Assess this cell for malaria.
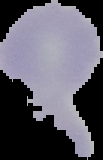
Uninfected.

preparation = thin blood smear
image size = 103×160 pixels
image type = segmented cell region with the area outside set to black